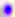
magnification: 400x
identification: Toxoplasma gondii
modality: photomicrograph